Assess the morphology of the erythrocytes.
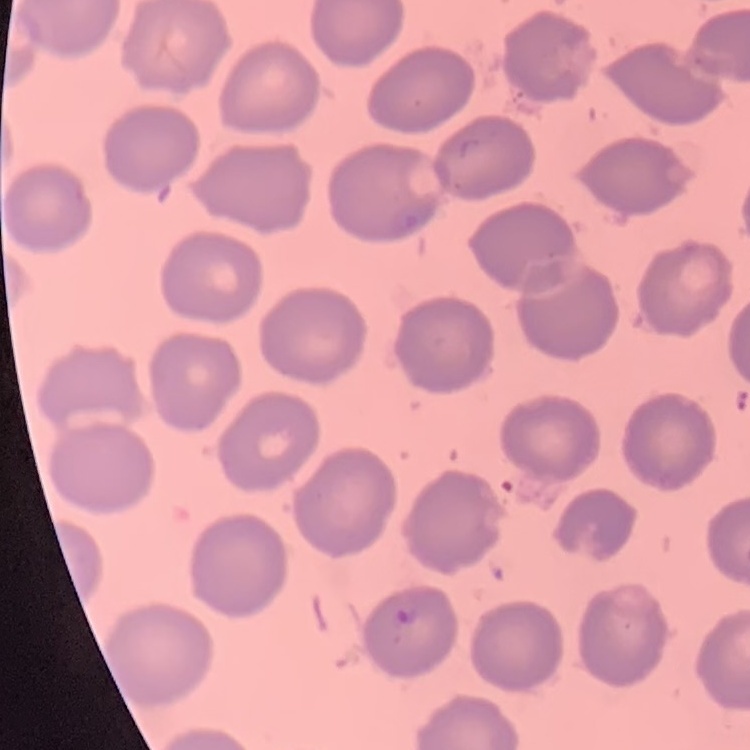

They show no rouleaux formation.

Summary:
  - Image type: one tile cut from a larger photomicrograph
  - Preparation: thin blood film
  - Stain: Field's or Giemsa